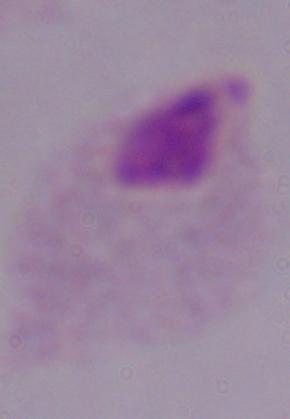

identification = trichomonad
modality = photomicrograph
magnification = 1000x